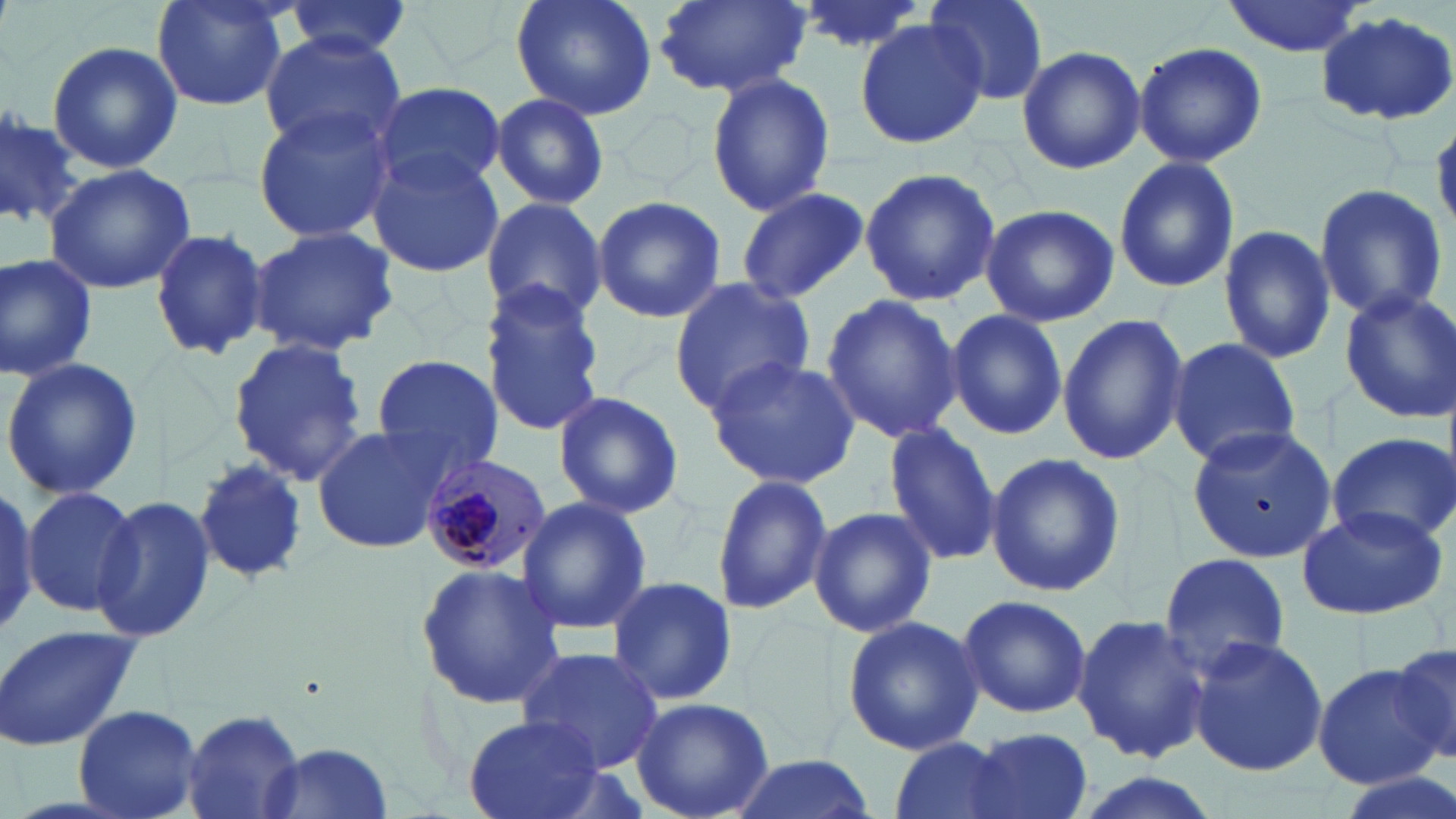
slide-level diagnosis = Plasmodium malariae
field of view = one of a larger specimen
Plasmodium malariae-infected red blood cell locations = approximate bounding boxes as (x1,y1)-(x2,y2) corner pairs in pixels: (416,452)-(548,574)
uninfected red blood cell locations = approximate bounding boxes as (x1,y1)-(x2,y2) corner pairs in pixels: (151,0)-(290,114), (511,0)-(658,122), (655,0)-(811,98), (790,0)-(930,56), (921,0)-(1050,106), (1219,0)-(1369,57), (282,1)-(413,59), (1315,10)-(1456,126), (852,17)-(987,151), (260,31)-(407,157), (47,41)-(182,176), (1133,41)-(1268,168), (1016,45)-(1146,175), (704,73)-(836,217), (372,81)-(506,194), (492,93)-(608,209), (250,104)-(397,243), (0,105)-(80,231), (1431,115)-(1456,230), (366,150)-(506,277), (1113,156)-(1241,293), (43,162)-(197,295), (860,167)-(1001,306), (1312,184)-(1448,322), (735,186)-(869,305), (478,195)-(609,325), (591,196)-(727,322), (979,204)-(1120,328), (248,224)-(401,356), (1218,225)-(1337,365), (149,228)-(268,360), (0,252)-(100,382), (667,278)-(816,410), (478,284)-(607,436), (1338,288)-(1455,423), (820,295)-(963,443), (946,308)-(1066,440), (1056,312)-(1187,466), (226,335)-(369,486), (1165,336)-(1301,468), (2,355)-(144,501), (370,355)-(507,478), (703,355)-(861,489), (551,390)-(685,519), (881,422)-(1002,566), (311,424)-(449,556), (1186,424)-(1336,560), (1327,432)-(1456,549), (983,452)-(1124,596), (191,458)-(310,584), (712,474)-(833,616), (0,484)-(38,639), (22,486)-(144,618), (97,495)-(220,642), (515,496)-(652,636), (808,504)-(938,636), (1297,504)-(1448,621), (1157,552)-(1293,680), (414,562)-(566,710), (605,575)-(738,708), (955,594)-(1093,719), (841,613)-(986,757), (1072,614)-(1213,765), (0,624)-(140,753), (1187,635)-(1328,777), (1387,641)-(1456,770), (517,647)-(666,774), (1313,664)-(1442,788), (630,697)-(773,819), (74,704)-(203,818), (182,705)-(307,817), (463,716)-(603,818), (972,729)-(1093,818), (886,737)-(1026,819), (258,742)-(397,818), (727,753)-(877,819), (1333,770)-(1456,819), (1064,772)-(1224,819)
magnification = 1000x
modality = light microscopy
preparation = thin blood film
stain = May-Grünwald-Giemsa
image size = 1456×819 pixels